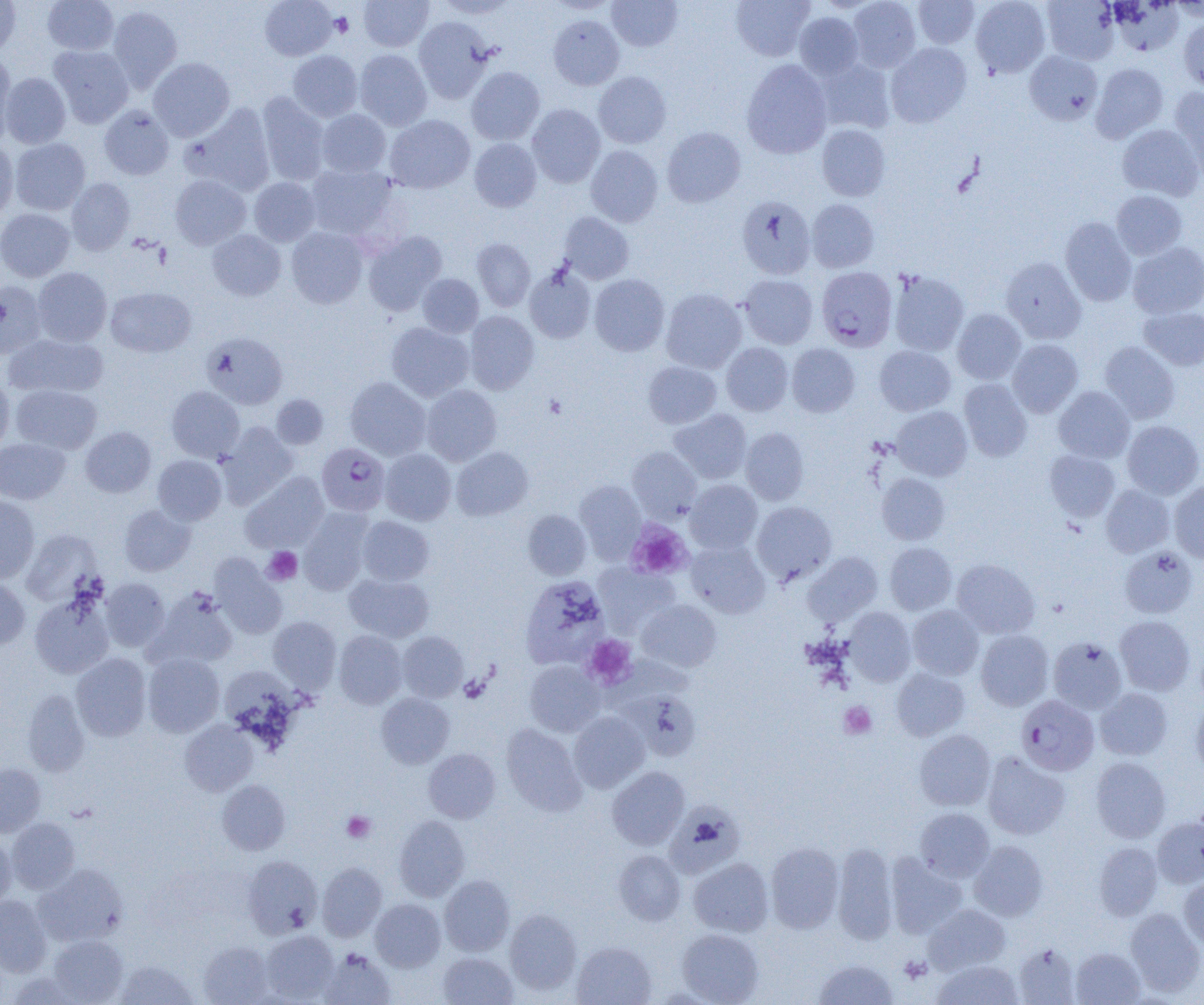

Summary:
  - Coordinate format: approximate bounding boxes as named x1/y1/x2/y2 corners in pixels
  - Plasmodium falciparum-infected red blood cell locations: (x1=817, y1=266, x2=898, y2=351), (x1=317, y1=442, x2=390, y2=515), (x1=1016, y1=695, x2=1099, y2=776)
  - Platelet locations: (x1=330, y1=12, x2=353, y2=36), (x1=544, y1=394, x2=567, y2=419), (x1=626, y1=520, x2=693, y2=579), (x1=263, y1=547, x2=302, y2=585), (x1=582, y1=635, x2=637, y2=689), (x1=838, y1=702, x2=876, y2=739), (x1=342, y1=811, x2=375, y2=843), (x1=898, y1=955, x2=931, y2=983)
  - Uninfected red blood cell locations: (x1=0, y1=0, x2=21, y2=57), (x1=42, y1=0, x2=119, y2=55), (x1=260, y1=0, x2=337, y2=60), (x1=358, y1=0, x2=433, y2=51), (x1=435, y1=0, x2=517, y2=18), (x1=546, y1=0, x2=619, y2=14), (x1=607, y1=0, x2=683, y2=51), (x1=731, y1=0, x2=815, y2=61), (x1=847, y1=0, x2=921, y2=72), (x1=914, y1=0, x2=979, y2=48), (x1=970, y1=0, x2=1050, y2=78), (x1=1041, y1=0, x2=1119, y2=64), (x1=1109, y1=1, x2=1184, y2=56), (x1=1169, y1=1, x2=1204, y2=21), (x1=106, y1=5, x2=182, y2=92), (x1=794, y1=12, x2=863, y2=79), (x1=548, y1=15, x2=624, y2=90), (x1=414, y1=17, x2=494, y2=102), (x1=1179, y1=17, x2=1204, y2=92), (x1=886, y1=43, x2=971, y2=127), (x1=49, y1=45, x2=134, y2=127), (x1=288, y1=50, x2=363, y2=121), (x1=354, y1=50, x2=432, y2=130), (x1=1025, y1=51, x2=1103, y2=125), (x1=0, y1=52, x2=17, y2=145), (x1=148, y1=57, x2=235, y2=141), (x1=741, y1=59, x2=832, y2=159), (x1=817, y1=59, x2=895, y2=133), (x1=1091, y1=63, x2=1169, y2=142), (x1=466, y1=66, x2=545, y2=145), (x1=593, y1=71, x2=671, y2=148), (x1=1, y1=73, x2=71, y2=148), (x1=1168, y1=88, x2=1204, y2=176), (x1=256, y1=92, x2=330, y2=185), (x1=182, y1=103, x2=276, y2=195), (x1=527, y1=104, x2=605, y2=188), (x1=99, y1=105, x2=174, y2=180), (x1=316, y1=109, x2=391, y2=177), (x1=385, y1=115, x2=475, y2=194), (x1=816, y1=124, x2=890, y2=201), (x1=1117, y1=124, x2=1203, y2=201), (x1=662, y1=127, x2=746, y2=207), (x1=10, y1=138, x2=90, y2=215), (x1=469, y1=138, x2=541, y2=211), (x1=0, y1=141, x2=17, y2=222), (x1=586, y1=145, x2=663, y2=227), (x1=306, y1=164, x2=397, y2=240), (x1=170, y1=175, x2=251, y2=249), (x1=67, y1=178, x2=135, y2=255), (x1=249, y1=178, x2=320, y2=246), (x1=1111, y1=190, x2=1187, y2=260), (x1=736, y1=195, x2=816, y2=279), (x1=807, y1=199, x2=879, y2=272), (x1=0, y1=209, x2=75, y2=281), (x1=559, y1=212, x2=634, y2=284), (x1=1060, y1=217, x2=1137, y2=306), (x1=287, y1=227, x2=368, y2=309), (x1=207, y1=229, x2=286, y2=300), (x1=363, y1=230, x2=447, y2=315), (x1=472, y1=238, x2=536, y2=310), (x1=1128, y1=241, x2=1204, y2=319), (x1=1001, y1=257, x2=1086, y2=343), (x1=33, y1=267, x2=112, y2=346), (x1=525, y1=267, x2=595, y2=343), (x1=889, y1=270, x2=969, y2=356), (x1=417, y1=273, x2=484, y2=338), (x1=589, y1=274, x2=669, y2=356), (x1=739, y1=274, x2=818, y2=349), (x1=0, y1=280, x2=46, y2=358), (x1=105, y1=287, x2=196, y2=358), (x1=661, y1=288, x2=747, y2=373), (x1=1138, y1=307, x2=1204, y2=370), (x1=952, y1=309, x2=1026, y2=384), (x1=465, y1=311, x2=539, y2=394), (x1=386, y1=321, x2=474, y2=401), (x1=202, y1=332, x2=287, y2=409), (x1=4, y1=333, x2=108, y2=398), (x1=1007, y1=339, x2=1083, y2=417), (x1=1099, y1=341, x2=1180, y2=424), (x1=721, y1=343, x2=793, y2=416), (x1=786, y1=344, x2=860, y2=417), (x1=875, y1=345, x2=956, y2=416), (x1=643, y1=361, x2=721, y2=428), (x1=0, y1=376, x2=14, y2=454), (x1=345, y1=376, x2=431, y2=461), (x1=959, y1=379, x2=1032, y2=461), (x1=11, y1=384, x2=102, y2=454), (x1=421, y1=385, x2=501, y2=466), (x1=167, y1=386, x2=244, y2=462), (x1=1053, y1=386, x2=1135, y2=463), (x1=271, y1=394, x2=328, y2=449), (x1=890, y1=406, x2=972, y2=481), (x1=670, y1=409, x2=752, y2=484), (x1=1122, y1=420, x2=1203, y2=499), (x1=217, y1=422, x2=299, y2=506), (x1=80, y1=426, x2=156, y2=497), (x1=740, y1=427, x2=809, y2=505), (x1=0, y1=437, x2=70, y2=504), (x1=451, y1=446, x2=534, y2=521), (x1=627, y1=446, x2=702, y2=522), (x1=379, y1=449, x2=456, y2=525), (x1=1044, y1=449, x2=1120, y2=521), (x1=153, y1=455, x2=226, y2=525), (x1=241, y1=472, x2=328, y2=552), (x1=876, y1=472, x2=950, y2=545), (x1=685, y1=480, x2=762, y2=553), (x1=1169, y1=480, x2=1204, y2=562), (x1=575, y1=481, x2=646, y2=561), (x1=1101, y1=484, x2=1175, y2=558), (x1=0, y1=495, x2=39, y2=583), (x1=752, y1=501, x2=837, y2=584), (x1=120, y1=504, x2=195, y2=576), (x1=300, y1=509, x2=373, y2=595), (x1=523, y1=510, x2=592, y2=580), (x1=357, y1=516, x2=434, y2=585), (x1=21, y1=529, x2=102, y2=605), (x1=686, y1=539, x2=770, y2=618), (x1=884, y1=542, x2=957, y2=615), (x1=1119, y1=546, x2=1198, y2=619), (x1=803, y1=552, x2=882, y2=626), (x1=210, y1=555, x2=287, y2=639), (x1=951, y1=559, x2=1040, y2=638), (x1=593, y1=563, x2=680, y2=636), (x1=344, y1=572, x2=434, y2=642), (x1=521, y1=575, x2=610, y2=671), (x1=0, y1=577, x2=30, y2=649), (x1=100, y1=578, x2=170, y2=651), (x1=149, y1=588, x2=238, y2=669), (x1=30, y1=590, x2=115, y2=679), (x1=636, y1=599, x2=722, y2=672), (x1=907, y1=605, x2=984, y2=680), (x1=844, y1=607, x2=916, y2=686), (x1=1115, y1=615, x2=1195, y2=696), (x1=268, y1=616, x2=342, y2=691), (x1=975, y1=629, x2=1054, y2=711), (x1=333, y1=630, x2=407, y2=708), (x1=398, y1=632, x2=468, y2=702), (x1=1048, y1=636, x2=1127, y2=714), (x1=71, y1=653, x2=151, y2=741), (x1=143, y1=654, x2=224, y2=737), (x1=525, y1=661, x2=605, y2=736), (x1=601, y1=662, x2=700, y2=715), (x1=891, y1=668, x2=970, y2=741), (x1=224, y1=671, x2=305, y2=747), (x1=1095, y1=688, x2=1173, y2=760), (x1=21, y1=689, x2=90, y2=776), (x1=376, y1=693, x2=455, y2=768), (x1=1191, y1=701, x2=1204, y2=778), (x1=613, y1=703, x2=703, y2=771), (x1=569, y1=711, x2=650, y2=792), (x1=180, y1=720, x2=257, y2=796), (x1=501, y1=723, x2=586, y2=815), (x1=914, y1=729, x2=996, y2=811), (x1=424, y1=748, x2=500, y2=823), (x1=982, y1=752, x2=1070, y2=840), (x1=1090, y1=757, x2=1170, y2=843), (x1=0, y1=764, x2=46, y2=836), (x1=607, y1=766, x2=690, y2=849), (x1=217, y1=780, x2=290, y2=855), (x1=664, y1=802, x2=744, y2=878), (x1=915, y1=808, x2=994, y2=881), (x1=394, y1=815, x2=470, y2=901), (x1=1151, y1=816, x2=1204, y2=888), (x1=6, y1=818, x2=80, y2=893), (x1=0, y1=836, x2=16, y2=909), (x1=969, y1=841, x2=1048, y2=921), (x1=765, y1=842, x2=844, y2=933), (x1=832, y1=842, x2=899, y2=944), (x1=1094, y1=842, x2=1163, y2=920), (x1=613, y1=850, x2=686, y2=925), (x1=885, y1=854, x2=967, y2=938), (x1=243, y1=856, x2=322, y2=938), (x1=688, y1=858, x2=773, y2=937), (x1=34, y1=863, x2=127, y2=947), (x1=317, y1=863, x2=386, y2=941), (x1=440, y1=875, x2=514, y2=956), (x1=1180, y1=875, x2=1204, y2=951), (x1=0, y1=895, x2=51, y2=976), (x1=371, y1=899, x2=445, y2=971), (x1=924, y1=904, x2=1010, y2=973), (x1=1124, y1=907, x2=1204, y2=996), (x1=505, y1=909, x2=582, y2=994), (x1=677, y1=929, x2=763, y2=1004), (x1=260, y1=930, x2=339, y2=1002), (x1=48, y1=935, x2=127, y2=1004), (x1=199, y1=941, x2=274, y2=1004), (x1=572, y1=942, x2=656, y2=1005), (x1=1013, y1=943, x2=1080, y2=1004), (x1=1070, y1=947, x2=1145, y2=1004), (x1=319, y1=948, x2=396, y2=1005), (x1=438, y1=952, x2=518, y2=1004), (x1=813, y1=958, x2=899, y2=1004), (x1=115, y1=959, x2=198, y2=1004), (x1=933, y1=960, x2=1023, y2=1005)
  - Slide-level diagnosis: Plasmodium falciparum
  - Modality: light microscopy
  - Field of view: one of a larger specimen
  - Image size: 1204×1005 pixels
  - Preparation: thin blood smear
  - Magnification: 1000x